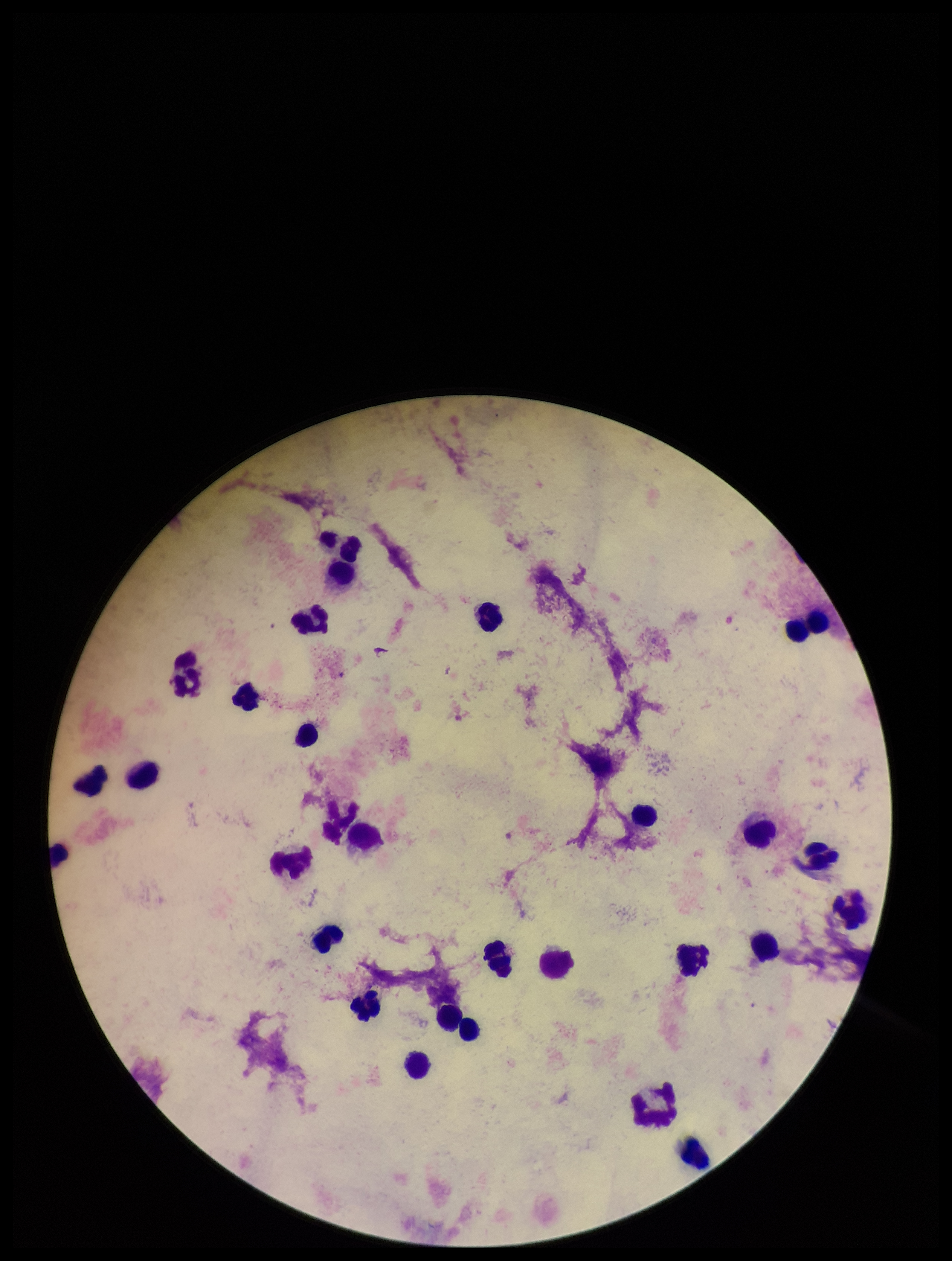

One field from this slide. Parasite count: 0. Giemsa stain. Preparation: thick blood smear. Image is 952×1261 pixels. Leukocyte count: 30. Photographed through the microscope eyepiece with a smartphone camera. Patient malaria status: negative. Plasmodium parasites: none identified.